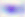
Summary:
  - Identification: Toxoplasma gondii
  - Modality: photomicrograph
  - Magnification: 400x